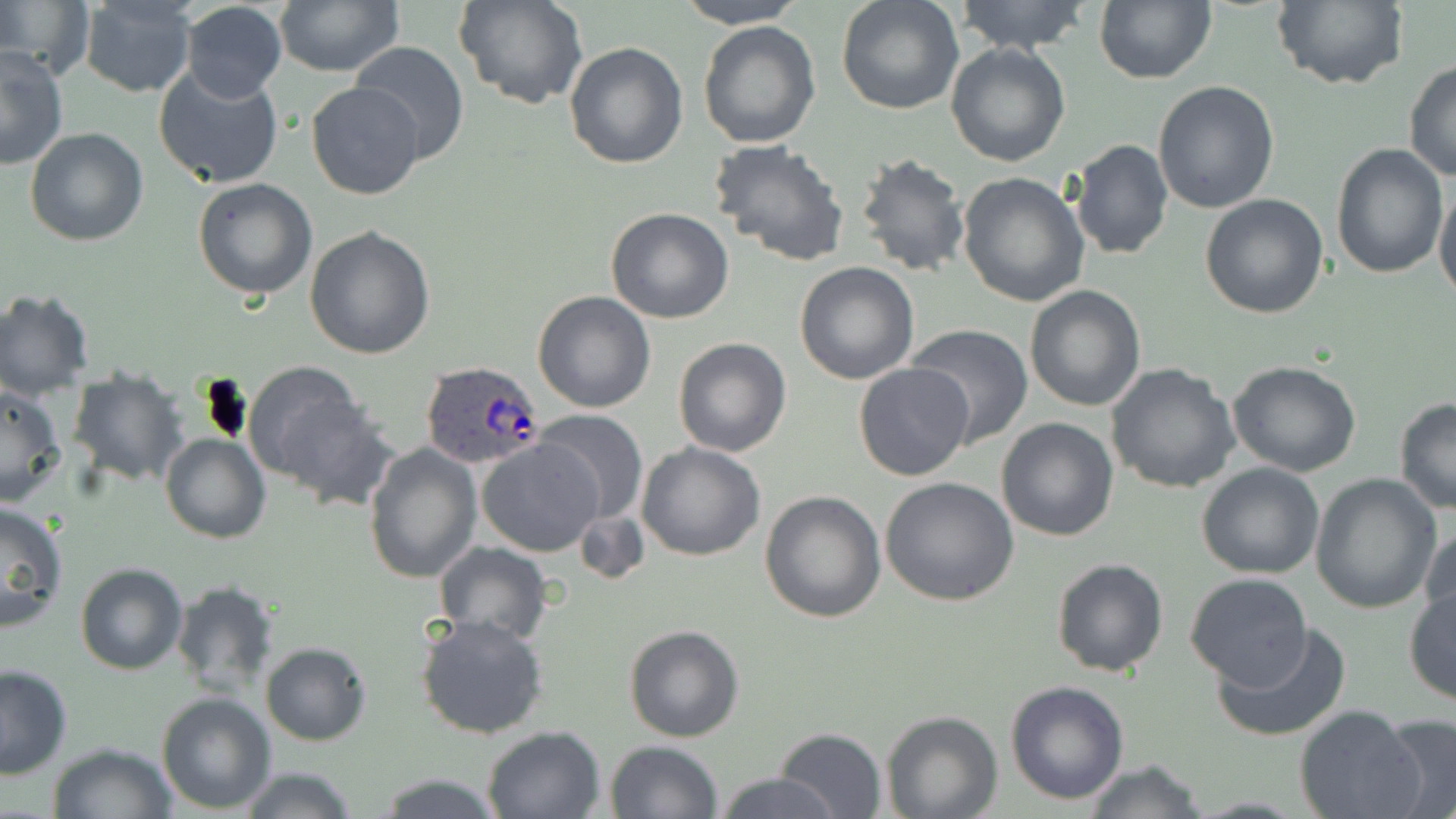

Approximate bounding boxes as (x1, y1, x2, y2) in pixels. Plasmodium ovale-infected red blood cell locations: (418, 360, 543, 472). Uninfected red blood cell locations: (274, 0, 402, 76), (456, 0, 586, 110), (674, 0, 807, 29), (835, 0, 964, 116), (953, 0, 1095, 54), (1094, 0, 1216, 84), (1270, 0, 1406, 91), (0, 1, 90, 79), (77, 1, 197, 97), (179, 2, 288, 103), (697, 20, 821, 149), (347, 41, 471, 166), (563, 43, 688, 169), (946, 43, 1072, 167), (0, 47, 69, 169), (1404, 61, 1456, 184), (153, 63, 286, 189), (1152, 79, 1280, 215), (306, 81, 424, 200), (24, 127, 148, 246), (709, 137, 850, 267), (1069, 139, 1172, 260), (1330, 145, 1448, 281), (855, 151, 972, 279), (957, 171, 1091, 307), (192, 177, 318, 300), (1434, 185, 1456, 303), (1199, 193, 1329, 319), (605, 207, 735, 325), (304, 225, 437, 360), (795, 261, 921, 385), (1024, 285, 1147, 411), (0, 288, 95, 399), (532, 290, 656, 412), (905, 324, 1033, 445), (673, 337, 792, 456), (1228, 361, 1362, 477), (1106, 363, 1240, 496), (854, 364, 974, 482), (242, 365, 374, 498), (67, 366, 189, 487), (0, 384, 66, 506), (1393, 397, 1456, 513), (533, 409, 648, 527), (995, 417, 1121, 540), (161, 433, 270, 544), (477, 438, 602, 555), (364, 440, 482, 584), (636, 442, 766, 562), (1196, 463, 1325, 581), (1309, 474, 1443, 613), (880, 476, 1021, 608), (759, 490, 886, 624), (0, 501, 70, 631), (573, 507, 649, 586), (1419, 523, 1455, 637), (433, 541, 553, 644), (1050, 558, 1170, 677), (75, 563, 188, 676), (1184, 573, 1313, 690), (170, 579, 279, 700), (1404, 586, 1456, 706), (416, 613, 548, 741), (1213, 620, 1353, 741), (624, 624, 745, 742), (260, 641, 371, 746), (0, 664, 73, 779), (1005, 681, 1130, 805), (156, 692, 276, 814), (1295, 707, 1425, 819), (880, 711, 1002, 819), (1379, 714, 1456, 819), (479, 725, 605, 819), (773, 727, 888, 818), (605, 740, 725, 819), (46, 741, 178, 819), (1082, 760, 1207, 819), (236, 767, 362, 819), (373, 772, 504, 818), (716, 772, 839, 818). Slide-level diagnosis: Plasmodium ovale. 1000x magnification. One field of a larger specimen. Thin blood smear. May-Grünwald-Giemsa stain. Light microscopy. Image is 1456×819 pixels.